Assess this cell for malaria.
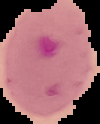
It is parasitized.

Image is 100×124 pixels. Cell region segmented out of the field of view; the surrounding area is masked to black. From a thin blood smear.